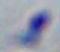
identification = Toxoplasma gondii
modality = micrograph
magnification = 1000x